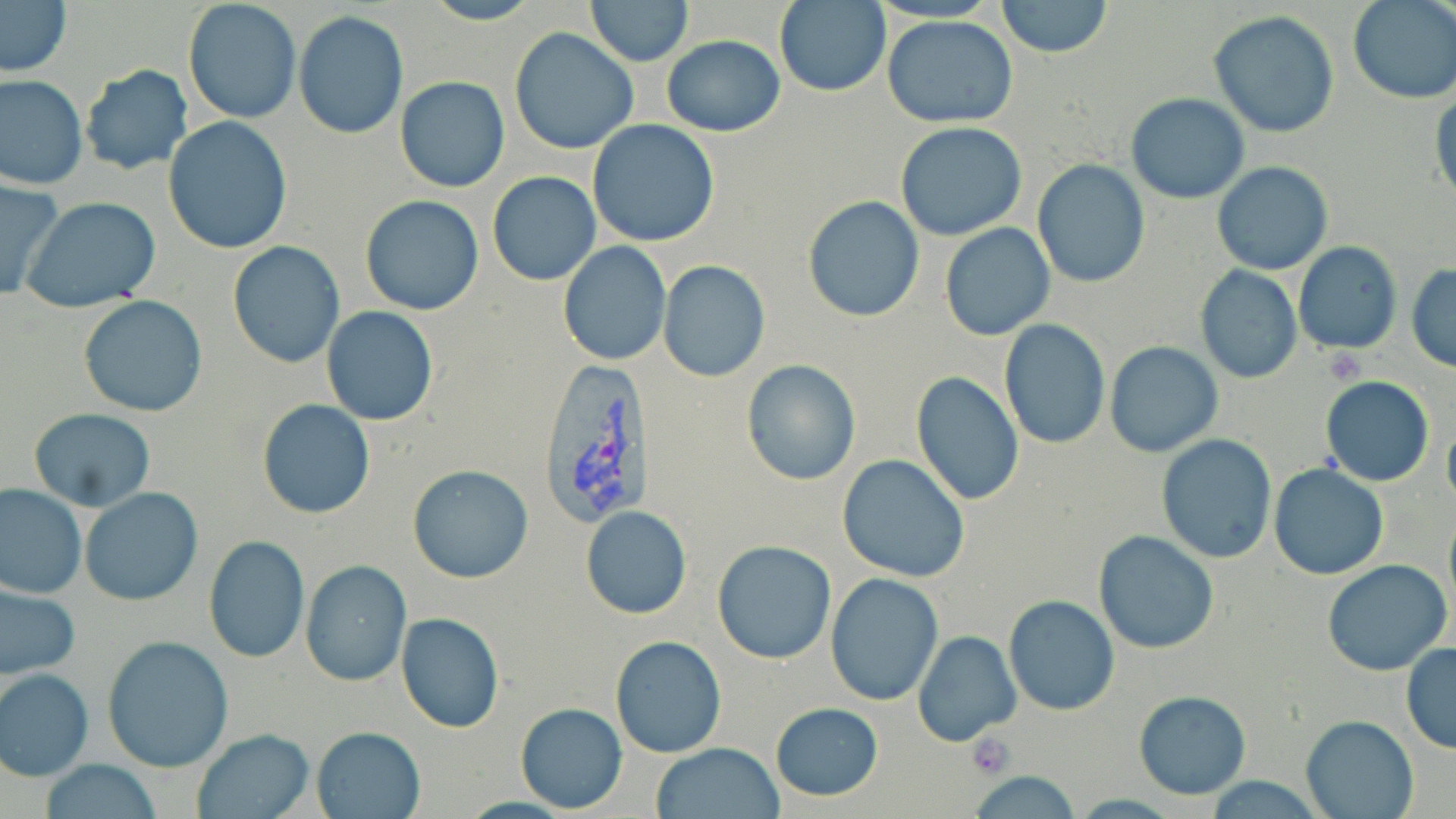

Approximate bounding boxes as [x1, y1, x2, y2] in pixels. Uninfected red blood cell locations: [418, 0, 543, 26], [587, 0, 691, 65], [996, 0, 1112, 57], [1348, 0, 1456, 103], [0, 1, 73, 78], [774, 1, 891, 97], [183, 2, 302, 122], [294, 11, 408, 140], [1209, 11, 1340, 139], [882, 15, 1020, 128], [509, 28, 639, 155], [661, 34, 785, 137], [79, 65, 194, 176], [0, 74, 88, 189], [396, 76, 510, 193], [1126, 92, 1250, 204], [163, 116, 293, 254], [587, 120, 720, 248], [896, 122, 1026, 240], [1031, 160, 1150, 288], [1211, 162, 1332, 276], [486, 172, 601, 287], [0, 179, 64, 301], [360, 194, 486, 315], [801, 196, 926, 322], [21, 197, 162, 314], [939, 222, 1055, 341], [227, 240, 346, 368], [557, 241, 671, 366], [1292, 241, 1403, 355], [658, 260, 771, 382], [1407, 264, 1456, 371], [1196, 266, 1302, 384], [77, 295, 208, 418], [322, 307, 438, 426], [999, 319, 1108, 449], [1104, 342, 1223, 458], [740, 358, 862, 485], [912, 371, 1026, 506], [1320, 376, 1436, 487], [256, 401, 377, 519], [27, 409, 156, 511], [1444, 419, 1456, 512], [1157, 435, 1277, 563], [837, 454, 970, 582], [407, 463, 535, 584], [1270, 464, 1388, 580], [1, 484, 86, 598], [79, 487, 202, 606], [579, 505, 693, 619], [1443, 508, 1456, 620], [1093, 529, 1219, 654], [202, 536, 310, 663], [713, 540, 836, 664], [1321, 559, 1452, 677], [300, 561, 412, 686], [825, 573, 942, 705], [0, 582, 80, 683], [1004, 594, 1118, 715], [396, 612, 504, 732], [914, 630, 1022, 747], [102, 635, 235, 772], [611, 636, 726, 756], [1400, 643, 1456, 752], [1, 667, 95, 780], [1133, 690, 1251, 799], [515, 702, 627, 813], [769, 702, 885, 800], [1301, 715, 1417, 819], [311, 726, 425, 818], [186, 729, 314, 818], [652, 742, 784, 819], [38, 760, 164, 817], [969, 769, 1084, 817], [1204, 776, 1326, 817]. Platelet locations: [1322, 347, 1365, 384], [967, 734, 1016, 778]. Plasmodium vivax-infected red blood cell locations: [534, 359, 660, 529]. Slide-level diagnosis: Plasmodium vivax. Thin blood smear. One field of a larger specimen. May-Grünwald-Giemsa-stained preparation. 1000x magnification. Image is 1456×819 pixels. Light microscopy.